Point out each Plasmodium parasite.
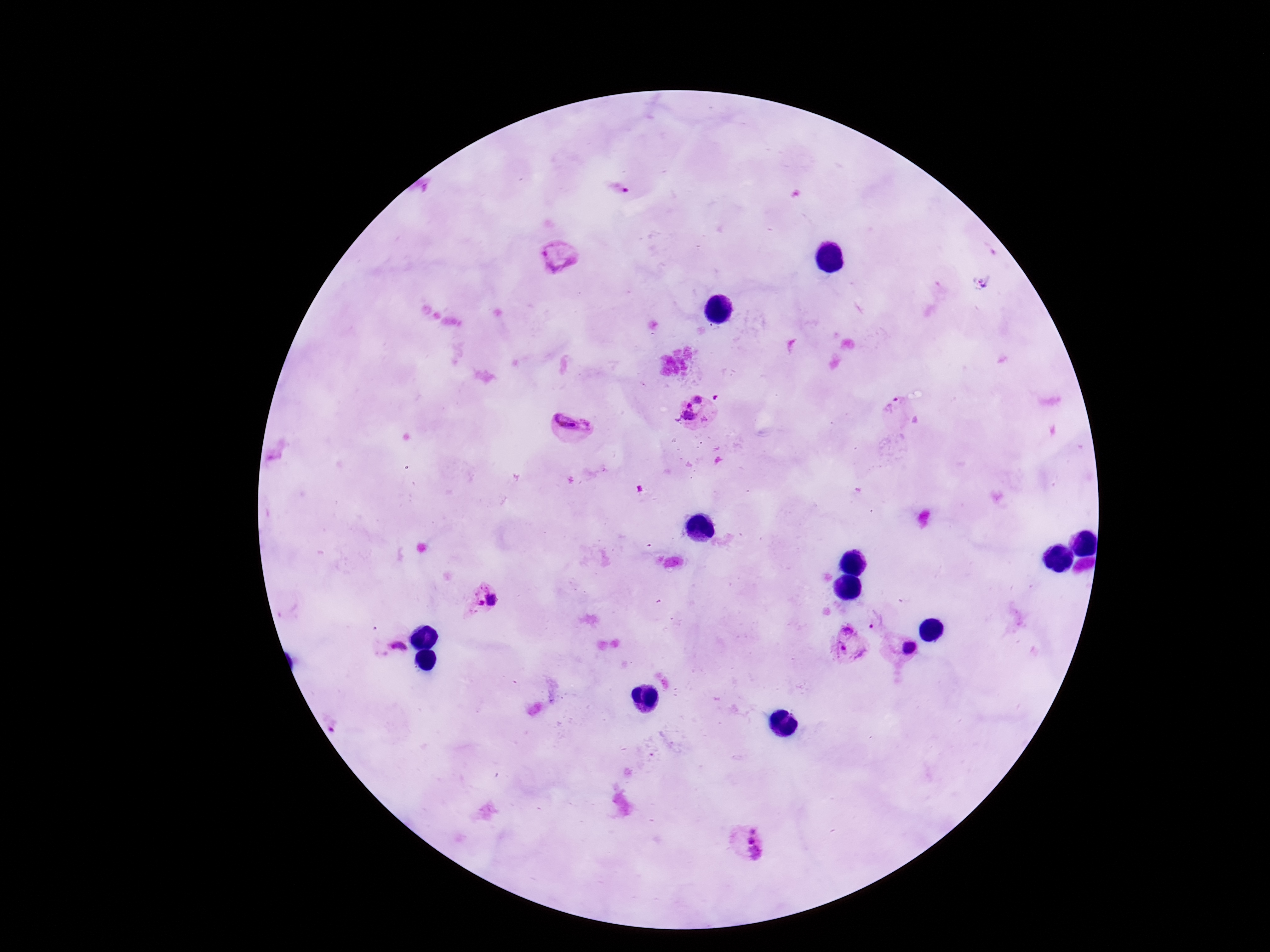

Approximate centers as {x, y} in pixels.
Plasmodium parasites: {617, 192}, {559, 257}, {982, 281}, {895, 409}, {697, 415}, {573, 427}, {483, 598}, {876, 620}, {394, 644}, {848, 644}, {906, 649}, {742, 841}.

stain = Giemsa
preparation = thick blood film
magnification = 100x
image size = 1270×952 pixels
patient malaria status = positive
field of view = one from this slide
capture = smartphone camera through the microscope eyepiece